Identify the cell.
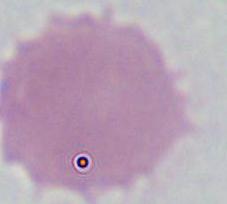
This is an erythrocyte.

Summary:
  - Modality: micrograph
  - Magnification: 1000x